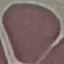
Summary:
  - Malaria status: uninfected
  - Stain: Giemsa
  - Capture: smartphone through the microscope eyepiece
  - Image type: automatically extracted cell patch, resized to 64 × 64 pixels
  - Preparation: thin blood film